Comment on the morphology of the red blood cells.
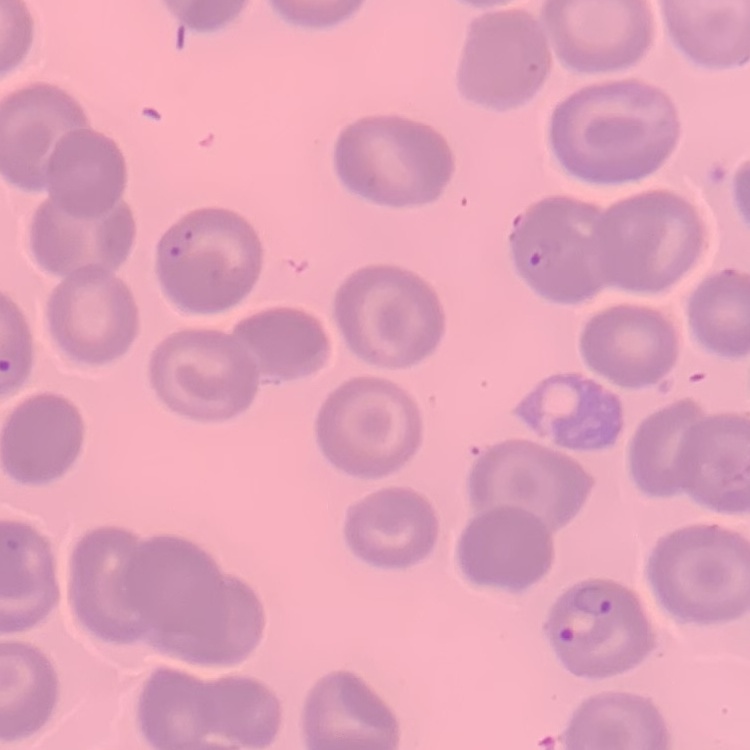

They show no rouleaux formation.

preparation: thin blood film
image_type: square crop of a larger photomicrograph
stain: Field's or Giemsa